Give the position of every leukocyte visible.
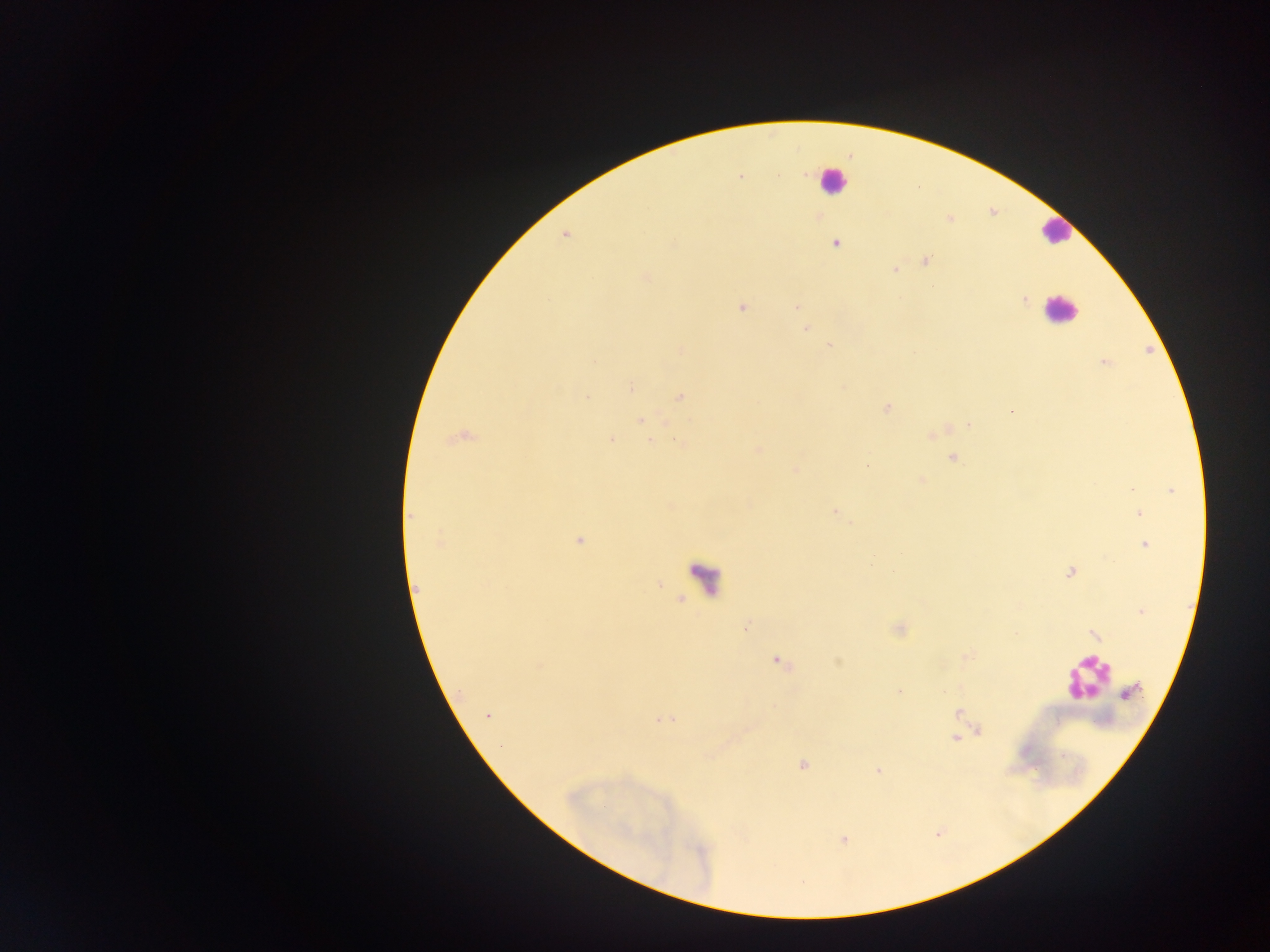

Approximate centers as [x, y] in pixels.
Leukocytes: [832, 180], [1054, 231], [1060, 310], [1086, 677].

Plasmodium parasite locations: [740, 176], [778, 176], [950, 220], [565, 234], [836, 243], [925, 262], [894, 269], [646, 277], [1024, 301], [741, 307], [796, 307], [805, 328], [829, 346], [681, 349], [1104, 362], [630, 388], [680, 396], [587, 397], [887, 408], [1012, 411], [640, 420], [968, 425], [460, 436], [931, 436], [611, 439], [650, 441], [680, 443], [758, 451], [952, 458], [868, 465], [796, 469], [921, 480], [1171, 491], [835, 510], [1139, 513], [411, 516], [579, 541], [441, 542], [1145, 545], [1070, 572], [1141, 611], [899, 629], [1093, 635], [777, 661], [898, 691], [1129, 692], [958, 712], [488, 715], [665, 720], [980, 732], [956, 738], [803, 765], [878, 770], [844, 840]. Single field of view. Photographed through a microscope with a mobile-phone camera. Sample from Ghana. Image is 1270×952 pixels. Thick blood film.